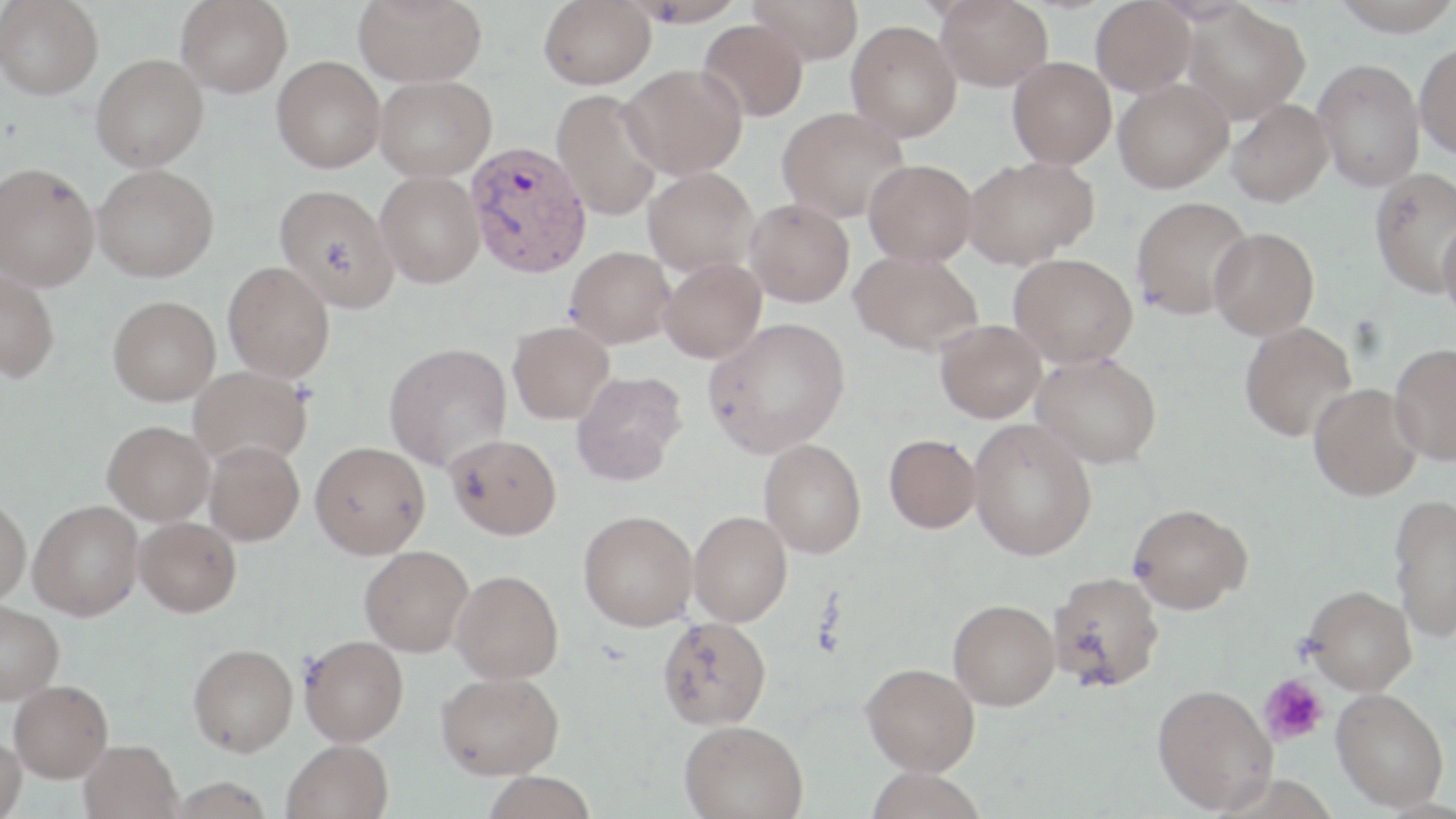

Approximate bounding boxes as (x1, y1, x2, y2) in pixels. Platelet locations: (1258, 673, 1329, 747). Plasmodium vivax-infected red blood cell locations: (466, 141, 592, 278). Uninfected red blood cell locations: (176, 0, 292, 98), (353, 0, 485, 87), (539, 0, 655, 89), (626, 0, 748, 27), (749, 0, 864, 65), (936, 0, 1053, 92), (1091, 0, 1196, 96), (1329, 0, 1456, 37), (0, 1, 103, 100), (1182, 3, 1310, 122), (698, 19, 808, 122), (846, 21, 962, 141), (1414, 41, 1456, 159), (91, 53, 208, 171), (272, 56, 385, 172), (1007, 56, 1116, 169), (1312, 58, 1424, 192), (621, 63, 748, 179), (375, 75, 496, 180), (1113, 78, 1233, 193), (552, 89, 664, 221), (1227, 99, 1334, 207), (776, 106, 909, 224), (963, 156, 1098, 268), (864, 159, 978, 266), (0, 162, 99, 290), (93, 165, 218, 282), (644, 167, 757, 276), (1369, 168, 1456, 298), (375, 171, 484, 288), (274, 183, 399, 312), (1131, 196, 1254, 320), (744, 198, 855, 307), (1438, 217, 1456, 326), (1209, 227, 1320, 340), (565, 246, 675, 348), (850, 250, 983, 356), (1009, 253, 1137, 367), (659, 258, 767, 363), (223, 261, 335, 383), (0, 269, 60, 383), (108, 295, 221, 405), (704, 317, 850, 458), (935, 320, 1046, 423), (1239, 321, 1357, 442), (508, 322, 615, 424), (384, 342, 512, 472), (1389, 342, 1456, 466), (1032, 352, 1162, 468), (189, 365, 311, 468), (571, 371, 687, 486), (1308, 384, 1423, 501), (969, 418, 1097, 560), (102, 420, 214, 525), (446, 434, 562, 540), (884, 434, 981, 533), (759, 438, 866, 558), (203, 440, 305, 545), (310, 441, 430, 558), (1388, 494, 1456, 642), (0, 496, 31, 606), (29, 500, 143, 620), (1128, 503, 1253, 614), (579, 510, 698, 631), (688, 511, 793, 626), (135, 517, 241, 616), (359, 545, 473, 657), (451, 570, 564, 684), (1049, 571, 1164, 692), (1303, 585, 1417, 695), (948, 598, 1060, 710), (0, 601, 63, 704), (657, 615, 772, 730), (299, 634, 409, 746), (188, 643, 298, 757), (861, 662, 980, 775), (436, 671, 564, 779), (9, 680, 113, 782), (1153, 683, 1278, 814), (1332, 688, 1449, 811), (678, 719, 808, 819), (0, 734, 26, 819), (282, 739, 394, 819), (79, 740, 183, 819), (865, 766, 986, 819), (482, 771, 597, 819), (168, 777, 274, 818). Slide-level diagnosis: Plasmodium vivax. One field of a larger specimen. May-Grünwald-Giemsa-stained preparation. Thin blood smear. Image is 1456×819 pixels. 1000x magnification. Light microscopy.